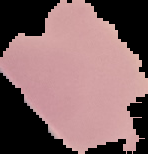

{
  "preparation": "thin blood smear",
  "image_size": "148×154 pixels",
  "image_type": "cell region segmented out of the field of view; surrounding area masked to black",
  "malaria_status": "uninfected"
}